Classify this cell by malaria status.
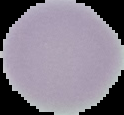

It is uninfected.

The area outside the segmented cell region is set to black. From a thin blood smear. Image is 124×115 pixels.